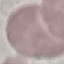
Result: negative for malaria parasites. Thin smear of blood. Automatically extracted cell patch, resized to 64 × 64 pixels. Photographed with a smartphone camera at the microscope eyepiece. Giemsa stain.